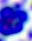

400x magnification. A leukocyte is seen. Micrograph.